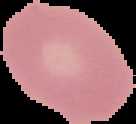

Summary:
  - Image size: 136×124 pixels
  - Preparation: thin blood smear
  - Image type: segmented cell region with the area outside set to black
  - Malaria status: uninfected